Report the malaria status of this cell.
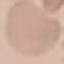

It is uninfected.

image_type: automatically extracted cell patch, resized to 64 × 64 pixels
capture: smartphone through the microscope eyepiece
preparation: thin smear
stain: Giemsa